Describe the morphology of the red blood cells.
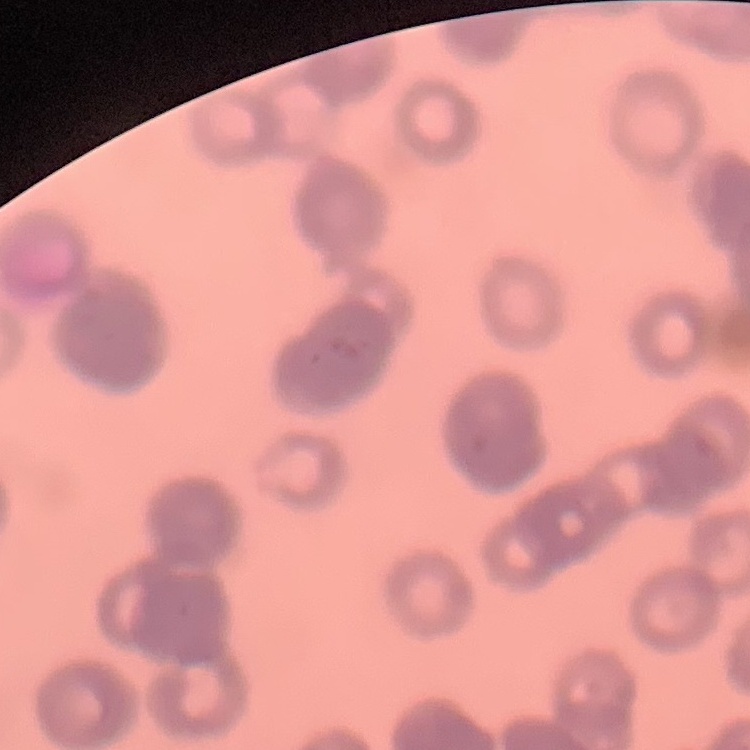
They show rouleaux formation.

stain: Field's or Giemsa
preparation: thin peripheral smear
image_type: square crop of a larger photomicrograph